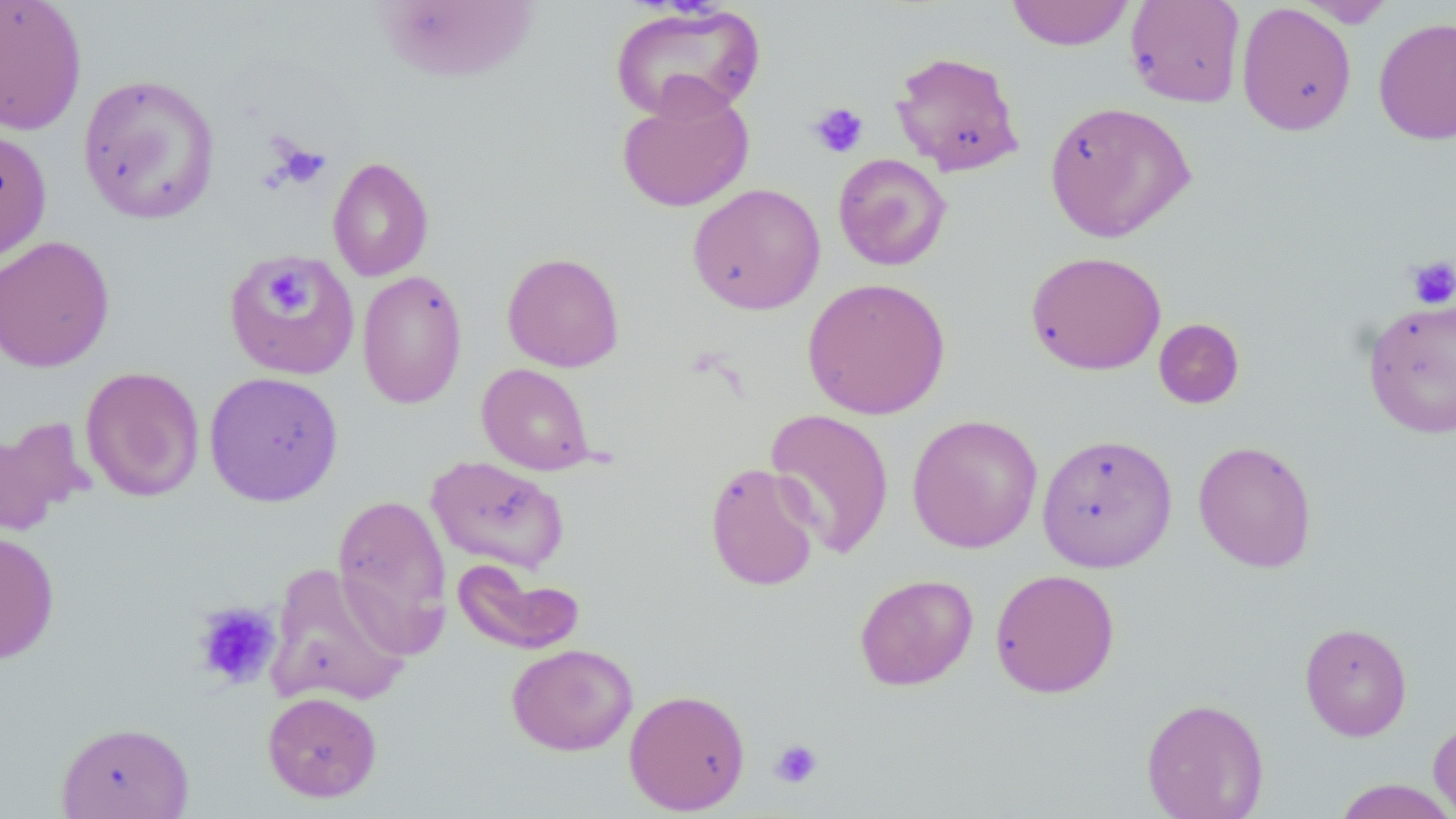
slide-level diagnosis = no evidence of blood parasites
stain = May-Grünwald-Giemsa
field of view = single
platelet locations = approximate bounding boxes as [x1, y1, x2, y2] in pixels: [808, 102, 869, 159], [273, 141, 331, 188], [1407, 256, 1456, 310], [266, 270, 308, 311], [192, 602, 281, 690], [769, 738, 823, 789]
modality = light microscopy
preparation = thin blood film
image size = 1456×819 pixels
uninfected red blood cell locations = approximate bounding boxes as [x1, y1, x2, y2] in pixels: [0, 0, 88, 136], [1004, 0, 1135, 51], [1124, 0, 1246, 108], [1294, 0, 1396, 27], [1236, 2, 1357, 136], [608, 3, 766, 123], [1373, 17, 1456, 145], [889, 50, 1025, 177], [77, 74, 221, 225], [616, 85, 755, 213], [1043, 101, 1196, 243], [0, 128, 52, 265], [832, 153, 952, 271], [327, 156, 434, 281], [687, 183, 826, 315], [0, 235, 115, 372], [1025, 250, 1166, 375], [223, 251, 360, 381], [502, 252, 625, 372], [356, 269, 467, 409], [801, 277, 951, 419], [1362, 297, 1456, 439], [1154, 318, 1245, 409], [476, 363, 596, 475], [80, 366, 205, 501], [204, 371, 344, 507], [764, 408, 895, 559], [906, 413, 1043, 554], [0, 416, 90, 535], [1036, 433, 1177, 573], [1193, 440, 1317, 572], [426, 455, 570, 574], [704, 462, 822, 591], [332, 494, 453, 654], [0, 530, 60, 663], [453, 559, 584, 656], [265, 563, 412, 708], [990, 568, 1120, 698], [854, 573, 978, 690], [1299, 622, 1413, 741], [506, 643, 638, 755], [623, 689, 751, 814], [262, 691, 383, 802], [1141, 697, 1269, 819], [1429, 716, 1456, 818], [56, 721, 195, 819], [1332, 779, 1456, 818]
magnification = 1000x